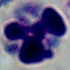

{
  "modality": "photomicrograph",
  "identification": "white blood cell",
  "magnification": "1000x"
}